Name the parasite shown.
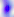

Toxoplasma gondii.

magnification = 400x
modality = micrograph